Locate every parasitized RBC.
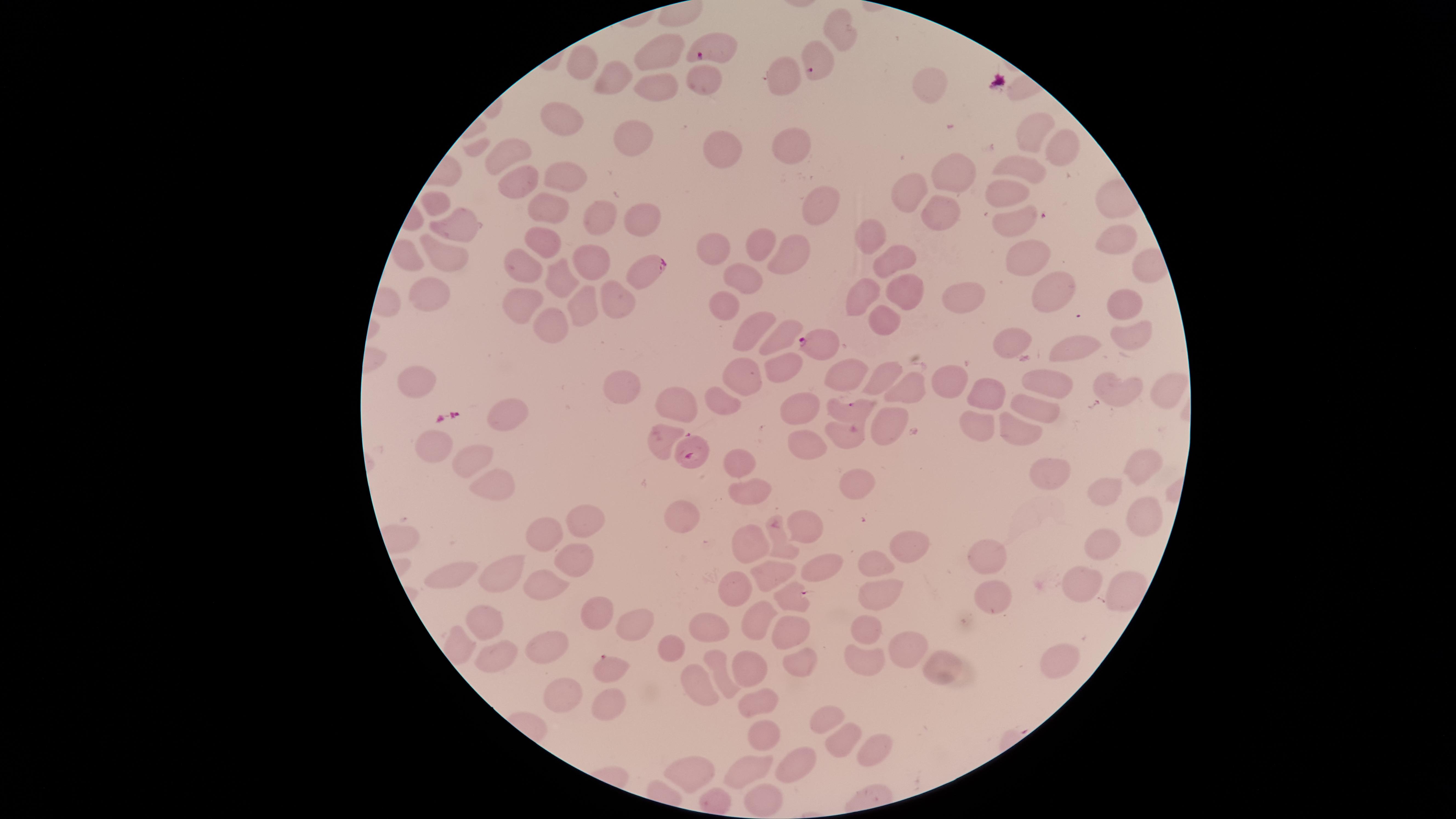

Approximate marker points as [x, y] in pixels.
Parasitized RBCs: [715, 50], [816, 64], [643, 269], [823, 344], [848, 407], [691, 451], [792, 594], [606, 666].

visible region = circular
preparation = thin blood film
uninfected RBCs = approximate marker points as [x, y] in pixels: [839, 28], [660, 49], [579, 67], [782, 75], [704, 76], [612, 79], [655, 85], [932, 85], [558, 115], [1032, 132], [630, 134], [792, 142], [720, 146], [1059, 148], [503, 156], [1026, 171], [562, 172], [950, 175], [522, 176], [913, 189], [1006, 189], [436, 204], [548, 205], [824, 208], [942, 214], [600, 217], [639, 218], [1017, 222], [459, 225], [873, 235], [1112, 242], [541, 243], [714, 243], [758, 245], [442, 253], [785, 256], [893, 256], [410, 259], [593, 260], [1024, 262], [518, 266], [742, 271], [552, 278], [1048, 290], [903, 293], [612, 295], [861, 295], [429, 297], [522, 301], [970, 302], [1121, 302], [581, 303], [723, 308], [883, 321], [549, 326], [747, 329], [1131, 329], [774, 338], [1008, 345], [1074, 349], [784, 369], [884, 370], [846, 375], [742, 379], [419, 380], [947, 380], [1160, 380], [910, 385], [1107, 385], [1052, 387], [621, 390], [987, 391], [721, 396], [672, 403], [1036, 405], [806, 406], [509, 415], [885, 422], [847, 431], [659, 435], [806, 443], [436, 445], [470, 455], [741, 459], [1143, 464], [1058, 470], [852, 481], [758, 483], [487, 485], [1106, 492], [1140, 517], [678, 519], [579, 522], [807, 527], [543, 536], [778, 538], [748, 540], [1101, 544], [903, 546], [998, 553], [575, 563], [870, 566], [453, 570], [815, 570], [507, 576], [766, 578], [1079, 581], [542, 588], [733, 591], [879, 592], [1005, 595], [1124, 595], [595, 613], [478, 616], [635, 619], [705, 622], [750, 627], [785, 631], [863, 631], [672, 644], [905, 647], [542, 648], [493, 650], [862, 655], [1059, 657], [797, 661], [940, 665], [749, 669], [724, 674], [695, 683], [557, 695], [601, 704], [751, 705], [824, 719], [762, 732], [836, 734], [876, 742], [795, 763], [750, 767], [694, 769], [714, 794], [763, 797]
image size = 1456×819 pixels
species = Plasmodium falciparum
stain = Giemsa
field of view = single
capture = smartphone photograph through the microscope eyepiece